Identify the parasite.
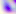
Toxoplasma gondii.

magnification: 400x
modality: micrograph